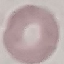

Result: no malaria parasites seen. Thin smear of blood. Photographed with a smartphone camera at the microscope eyepiece. Cell patch, automatically extracted from a larger field of view and resized to 64 × 64 pixels. Giemsa-stained preparation.